Name the parasite shown.
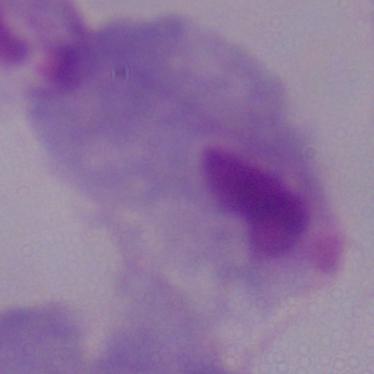

This is a trichomonad.

Photomicrograph. 1000x magnification.